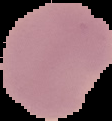 Segmented cell region on a black background. Malaria status: uninfected. From a thin blood film. Image is 112×121 pixels.